Name the cell type shown.
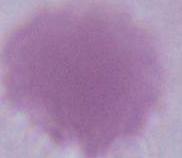
This is an erythrocyte.

Summary:
  - Modality: micrograph
  - Magnification: 1000x